Name the blood parasite species.
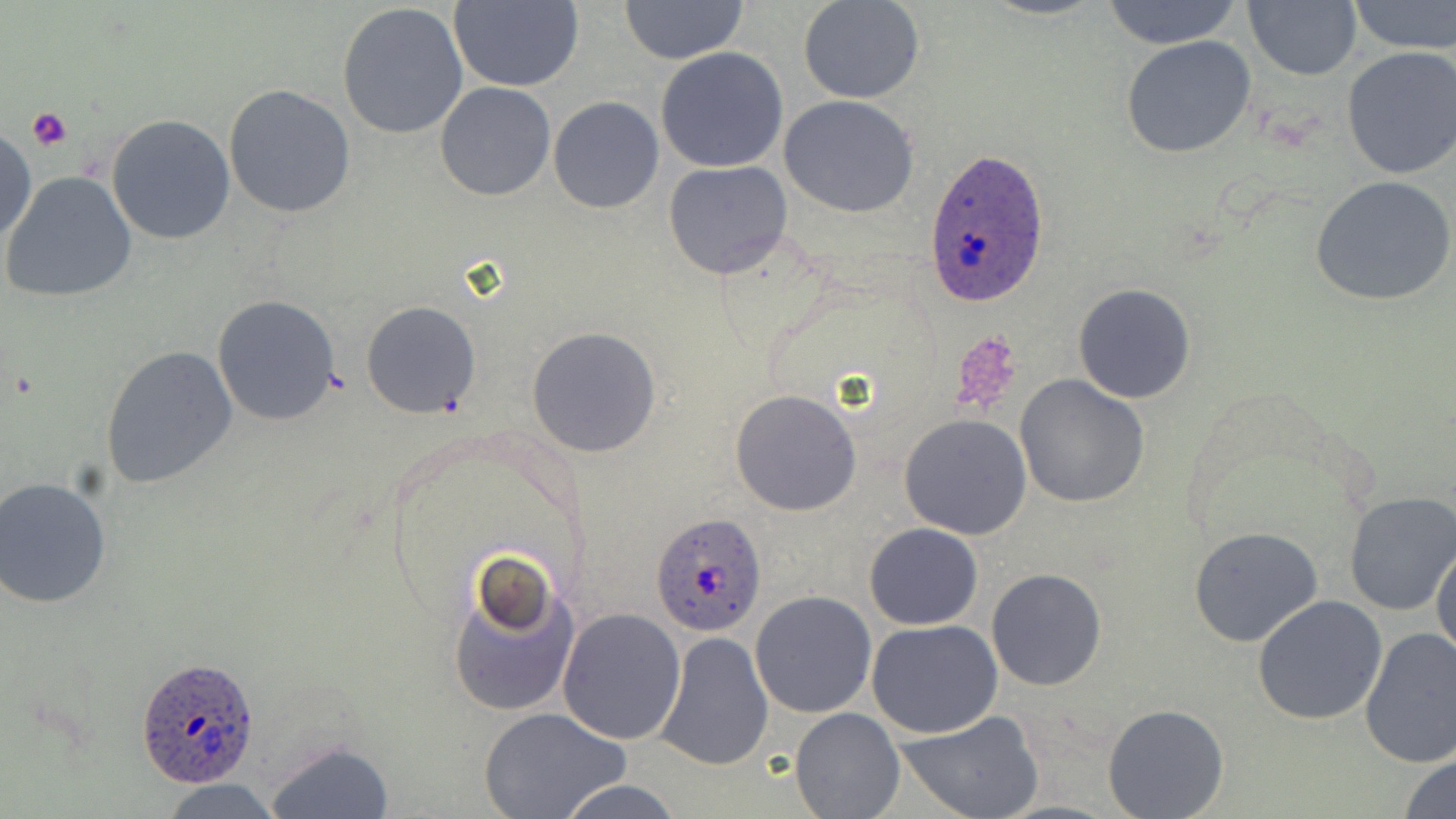
Plasmodium ovale.

{
  "image_size": "1456×819 pixels",
  "uninfected_red_blood_cell_locations": "approximate bounding boxes as (x1, y1, x2, y2) in pixels: (448, 0, 584, 90), (620, 0, 748, 65), (798, 0, 924, 103), (1099, 0, 1244, 49), (1244, 0, 1361, 81), (1346, 0, 1456, 54), (337, 2, 470, 141), (1120, 35, 1256, 158), (1340, 46, 1456, 181), (655, 47, 789, 173), (435, 81, 557, 201), (223, 83, 356, 218), (779, 95, 918, 217), (548, 96, 664, 214), (106, 114, 235, 245), (1, 123, 36, 248), (663, 160, 794, 280), (3, 171, 137, 303), (1310, 174, 1456, 309), (1073, 283, 1197, 404), (213, 295, 342, 426), (363, 301, 481, 417), (526, 326, 662, 458), (101, 345, 238, 491), (1015, 374, 1150, 508), (729, 388, 863, 517), (899, 413, 1033, 539), (1, 478, 115, 610), (1343, 491, 1456, 615), (864, 523, 983, 630), (1189, 527, 1324, 648), (1431, 535, 1456, 662), (448, 561, 579, 719), (986, 568, 1108, 692), (749, 591, 876, 719), (1252, 594, 1387, 724), (557, 606, 687, 744), (866, 619, 1002, 738), (1359, 627, 1456, 769), (653, 632, 774, 771), (1103, 703, 1230, 819), (790, 705, 904, 818), (481, 708, 629, 819), (894, 710, 1045, 819), (262, 739, 396, 818), (1398, 751, 1456, 819), (157, 778, 286, 818), (551, 778, 690, 819)",
  "magnification": "1000x",
  "stain": "May-Grünwald-Giemsa",
  "modality": "optical microscopy",
  "plasmodium_ovale_infected_red_blood_cell_locations": "approximate bounding boxes as (x1, y1, x2, y2) in pixels: (925, 144, 1053, 307), (650, 511, 767, 635), (138, 656, 261, 787)",
  "preparation": "thin blood film",
  "field_of_view": "single",
  "platelet_locations": "approximate bounding boxes as (x1, y1, x2, y2) in pixels: (26, 108, 72, 150), (948, 331, 1024, 415)"
}